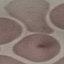
Summary:
  - Malaria status: uninfected
  - Preparation: thin blood smear
  - Capture: smartphone through the microscope eyepiece
  - Stain: Giemsa
  - Image type: automatically extracted cell patch, resized to 64 × 64 pixels